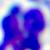

Captured at 400x magnification. Photomicrograph. A white blood cell is seen.